Name the parasite shown.
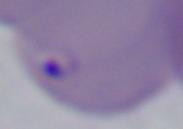

This is Babesia.

Photomicrograph. Captured at 1000x magnification.